Look for parasitized red blood cells.
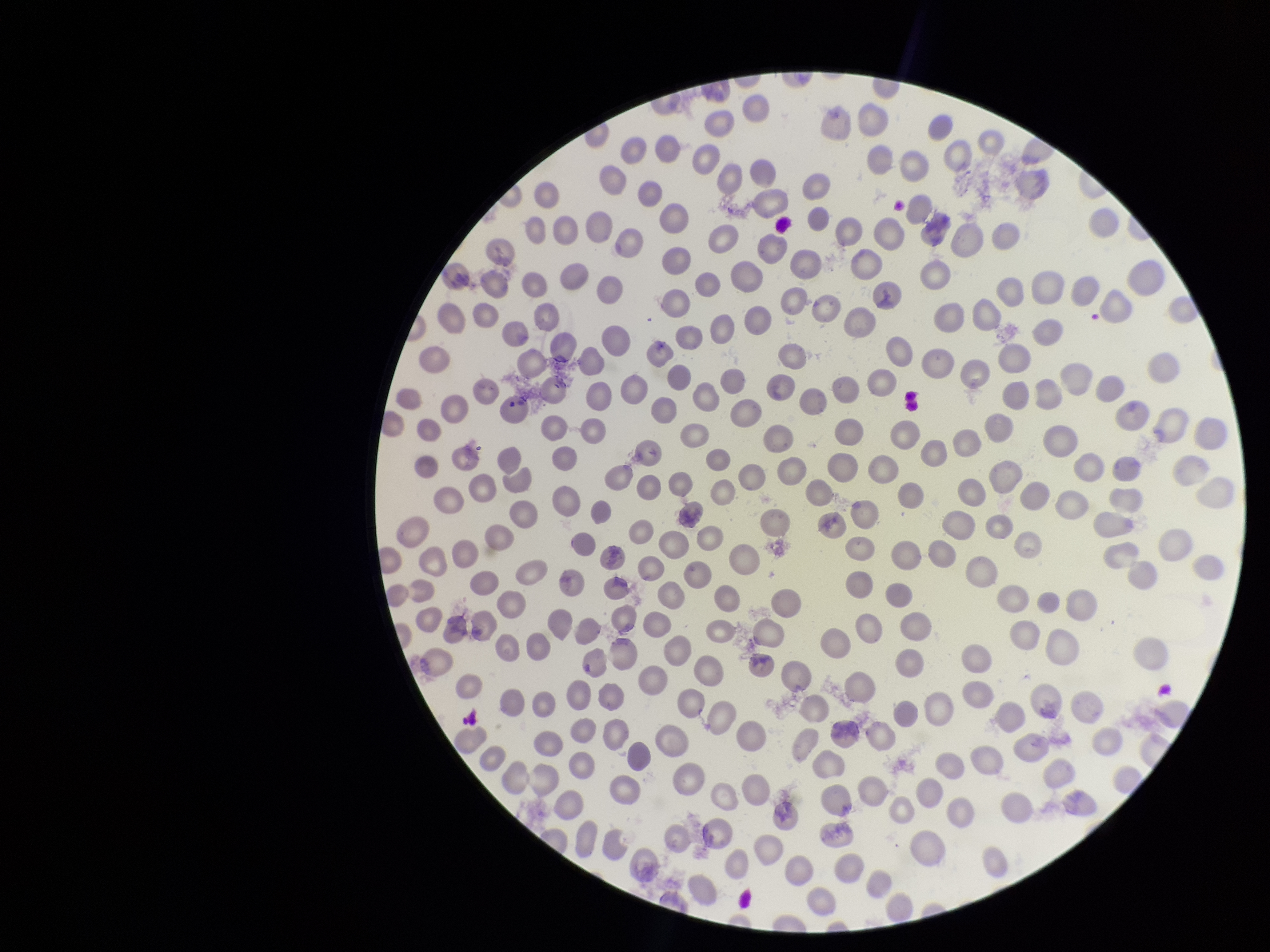

None detected.

Summary:
  - Capture: smartphone photograph through the microscope eyepiece
  - Patient malaria status: positive
  - Parasitized red blood cell count: 0
  - Red blood cell count: 271
  - Image size: 1270×952 pixels
  - Preparation: thin
  - Stain: Giemsa
  - Field of view: single
  - Species reported for this patient: Plasmodium vivax